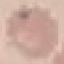
Result: no malaria parasites detected. Photographed with a smartphone camera at the microscope eyepiece. Thin blood smear. Cell patch, automatically extracted from a larger field of view and resized to 64 × 64 pixels. Giemsa stain.